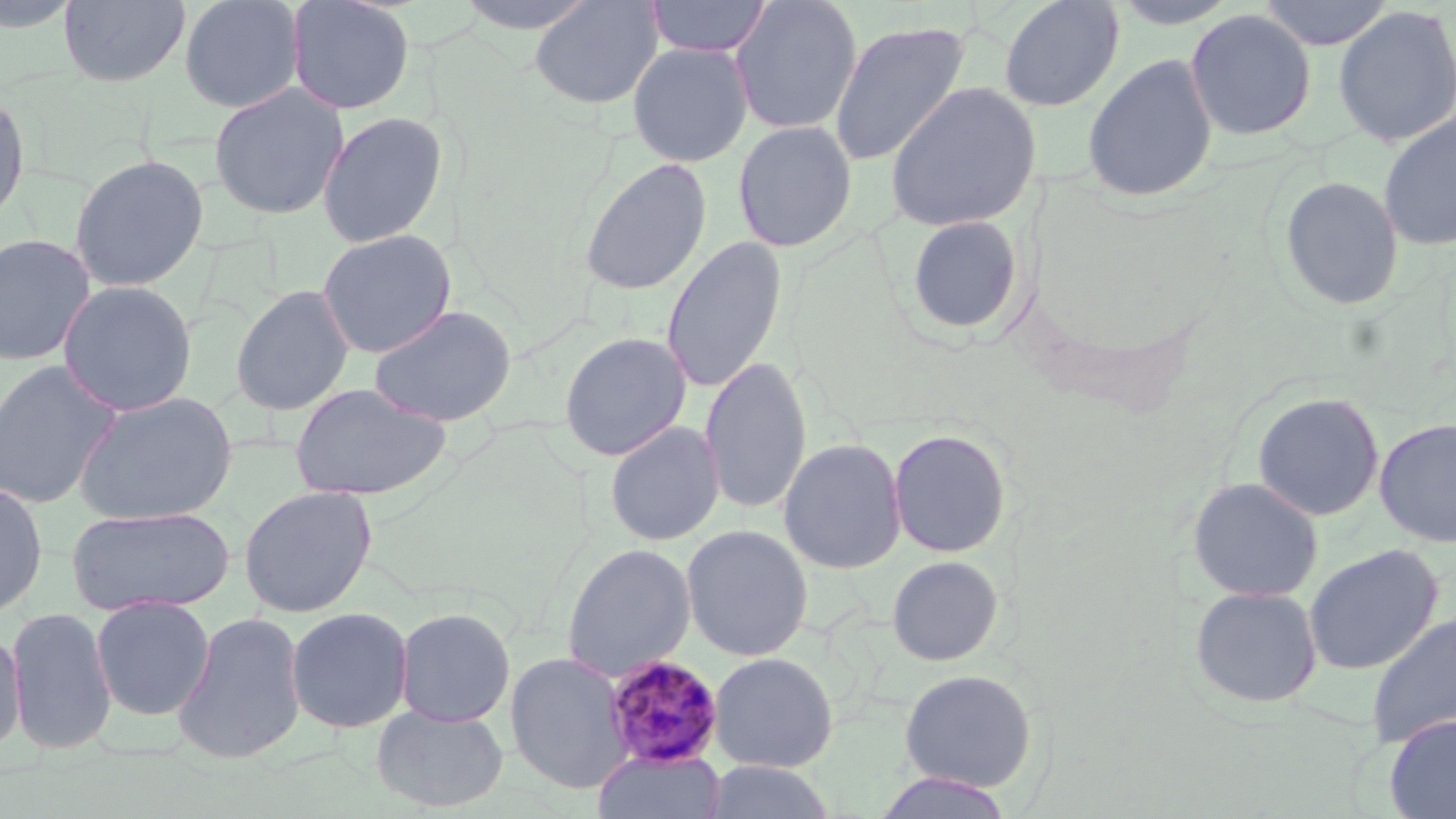

{
  "slide_level_diagnosis": "Plasmodium malariae",
  "stain": "May-Grünwald-Giemsa",
  "uninfected_red_blood_cell_locations": "approximate bounding boxes as (x1,y1)-(x2,y2) corner pairs in pixels: (0,0)-(86,33), (58,0)-(191,88), (178,0)-(305,113), (286,0)-(415,115), (452,0)-(603,35), (529,0)-(665,109), (645,0)-(772,58), (729,0)-(863,135), (997,0)-(1125,112), (1256,0)-(1394,50), (1332,4)-(1456,149), (1184,8)-(1317,141), (829,19)-(970,168), (627,42)-(753,167), (1081,53)-(1218,203), (884,80)-(1042,233), (208,82)-(348,220), (0,90)-(31,227), (316,111)-(448,248), (1377,111)-(1456,251), (732,120)-(857,252), (69,153)-(209,291), (578,156)-(712,296), (1279,175)-(1404,311), (904,214)-(1025,337), (316,228)-(456,358), (0,232)-(98,367), (660,235)-(788,394), (57,280)-(198,417), (231,284)-(355,416), (368,304)-(517,427), (558,331)-(692,461), (699,355)-(812,516), (0,358)-(125,511), (289,381)-(452,501), (73,391)-(238,526), (1252,391)-(1384,521), (1374,417)-(1456,548), (604,421)-(725,546), (888,428)-(1012,558), (777,437)-(907,575), (1186,476)-(1324,603), (0,480)-(48,619), (238,485)-(378,618), (67,506)-(235,617), (681,524)-(814,661), (561,542)-(696,682), (1303,544)-(1445,676), (886,555)-(1004,667), (1188,585)-(1323,710), (90,595)-(215,721), (6,606)-(117,755), (285,606)-(413,733), (394,607)-(516,727), (171,611)-(307,764), (1365,612)-(1456,748), (0,626)-(26,757), (504,650)-(632,793), (708,651)-(839,772), (898,668)-(1038,792), (371,704)-(510,813), (1384,714)-(1456,819), (593,748)-(725,819), (700,760)-(838,819), (872,772)-(1017,819)",
  "plasmodium_malariae_infected_red_blood_cell_locations": "approximate bounding boxes as (x1,y1)-(x2,y2) corner pairs in pixels: (603,654)-(725,769)",
  "field_of_view": "one of a larger specimen",
  "preparation": "thin blood film",
  "modality": "light microscopy",
  "image_size": "1456×819 pixels",
  "magnification": "1000x"
}